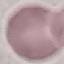

Summary:
  - Malaria status: uninfected
  - Image type: cell patch, automatically extracted from a larger field of view and resized to 64 × 64 pixels
  - Preparation: thin blood film
  - Stain: Giemsa
  - Capture: smartphone through the microscope eyepiece